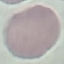
Summary:
  - Result: no malaria parasites detected
  - Image type: cell patch, automatically extracted from a larger field of view and resized to 64 × 64 pixels
  - Preparation: thin smear
  - Stain: Giemsa
  - Capture: smartphone through the microscope eyepiece